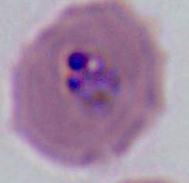

identification: Plasmodium
modality: micrograph
magnification: 400x or 1000x